Report the malaria status of this cell.
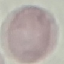
Uninfected.

Thin blood film. Giemsa stain. Acquired by smartphone through the microscope eyepiece. Cell patch, automatically extracted from a larger field of view and resized to 64 × 64 pixels.